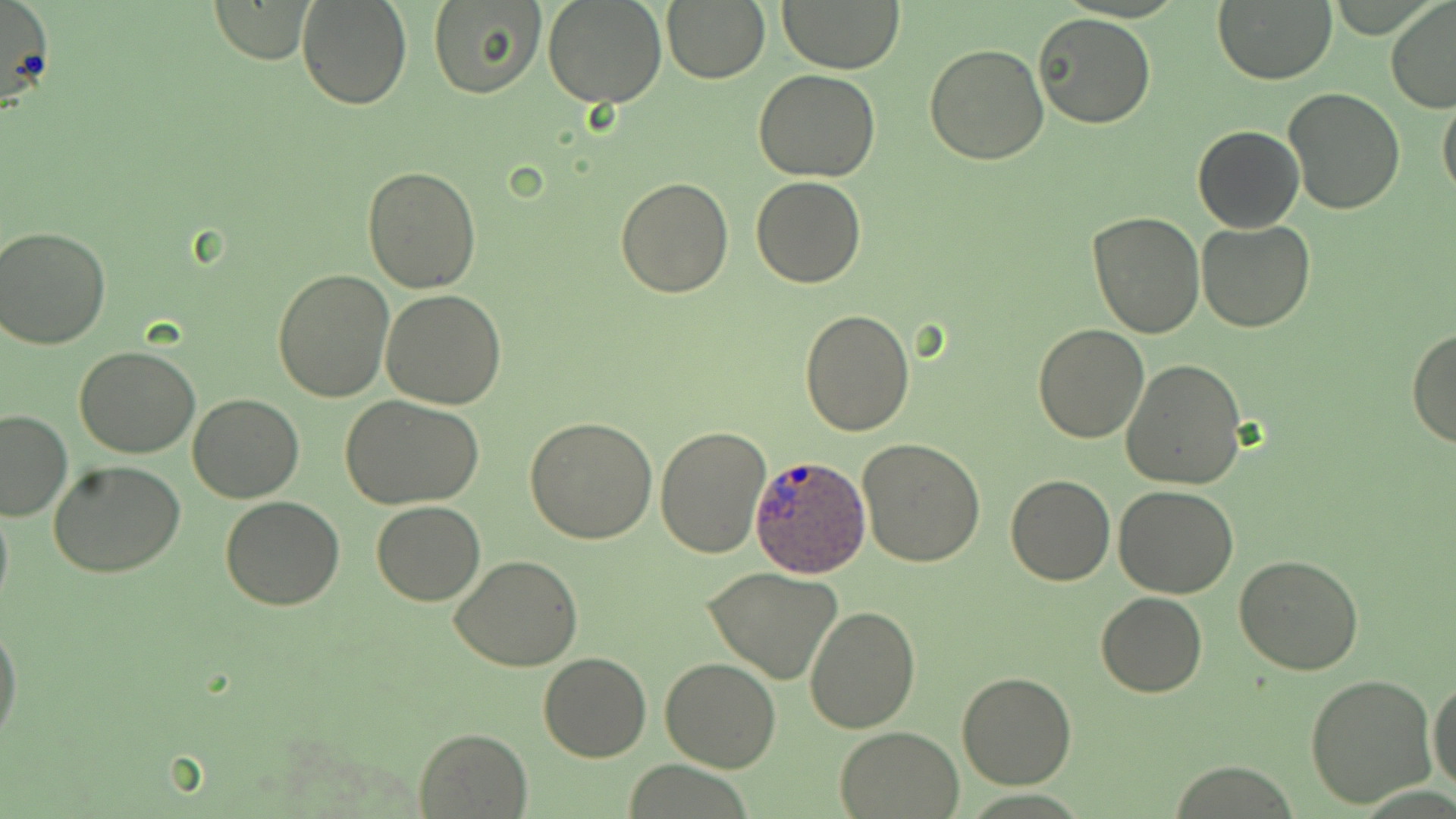
slide-level diagnosis = Plasmodium ovale
uninfected red blood cell locations = approximate bounding boxes as (x1, y1, x2, y2) in pixels: (0, 0, 56, 113), (296, 0, 413, 111), (428, 0, 546, 99), (542, 0, 669, 108), (661, 0, 770, 85), (778, 0, 906, 72), (1211, 0, 1338, 85), (1385, 0, 1456, 113), (208, 1, 315, 64), (1034, 12, 1155, 129), (924, 44, 1047, 165), (754, 69, 881, 182), (1280, 87, 1406, 215), (1437, 89, 1456, 203), (1193, 126, 1304, 232), (362, 165, 481, 293), (615, 176, 736, 297), (752, 177, 866, 289), (1086, 211, 1207, 338), (1196, 220, 1318, 332), (1, 226, 114, 348), (274, 268, 395, 403), (380, 288, 507, 409), (800, 309, 915, 437), (1033, 324, 1148, 442), (1409, 326, 1456, 449), (74, 344, 201, 458), (1121, 358, 1249, 489), (189, 394, 304, 504), (342, 396, 483, 510), (0, 409, 72, 521), (525, 415, 658, 543), (656, 425, 773, 558), (858, 439, 985, 569), (49, 461, 189, 578), (1006, 474, 1114, 586), (1114, 486, 1240, 598), (0, 492, 13, 621), (221, 494, 345, 610), (371, 500, 485, 605), (451, 555, 584, 672), (1234, 556, 1363, 675), (704, 563, 845, 684), (1096, 591, 1207, 698), (805, 606, 920, 734), (0, 617, 23, 749), (538, 652, 652, 762), (660, 655, 782, 772), (955, 673, 1076, 790), (1303, 673, 1436, 810), (1429, 677, 1456, 797), (834, 725, 964, 817), (414, 729, 532, 818), (1166, 762, 1305, 818)
field of view = single
preparation = thin blood smear
modality = light microscopy
magnification = 1000x
Plasmodium ovale-infected red blood cell locations = approximate bounding boxes as (x1, y1, x2, y2) in pixels: (749, 454, 871, 575)
image size = 1456×819 pixels
stain = May-Grünwald-Giemsa